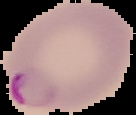
Result: Plasmodium parasites detected. Segmented cell region on a black background. Image is 136×115 pixels. From a thin blood film.